Outline each blood parasite and name the species.
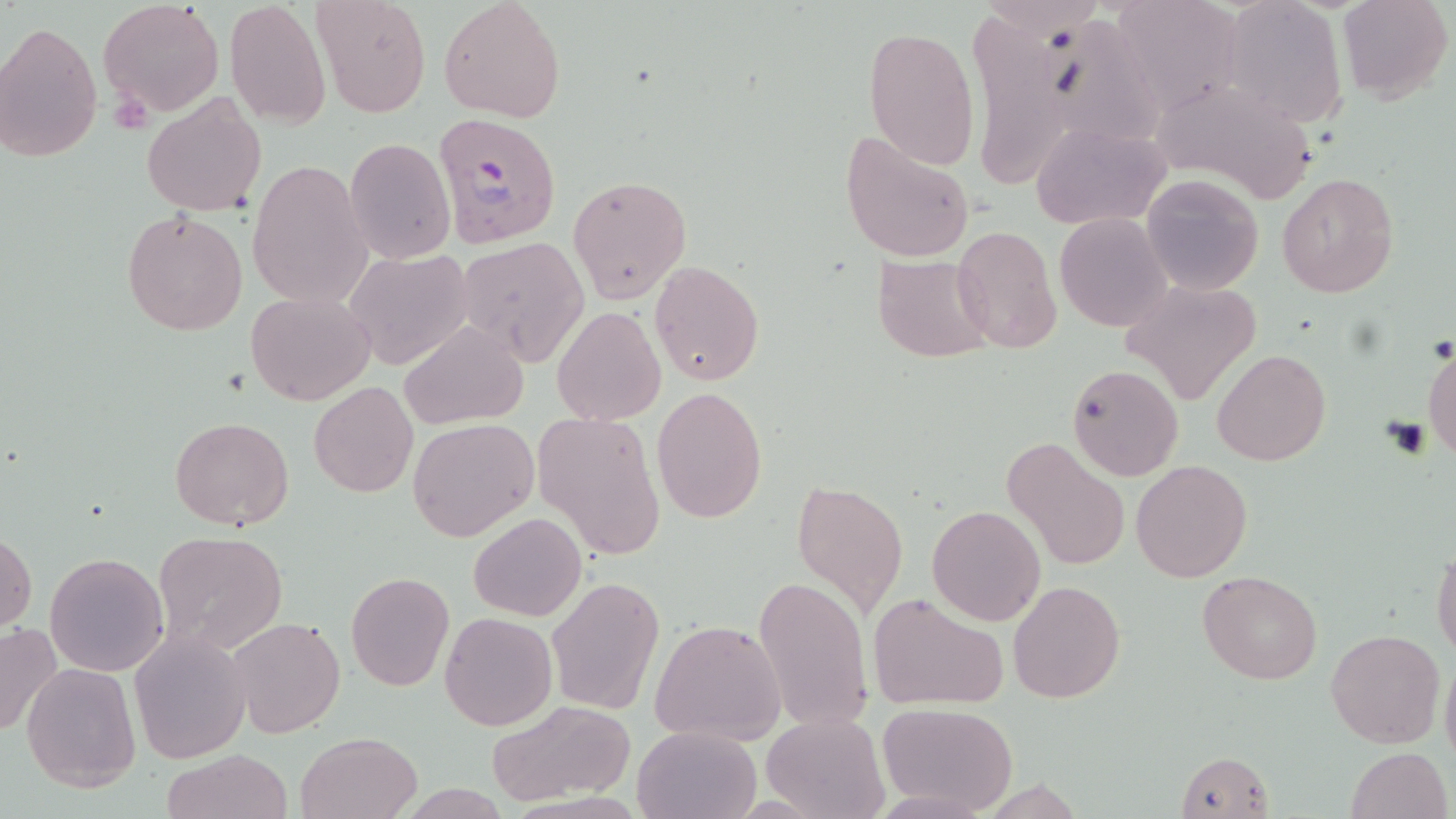
Approximate bounding boxes as (x1,y1)-(x2,y2) corner pairs in pixels.
Plasmodium falciparum-infected red blood cells: (431,110)-(561,249).
No Plasmodium ovale, Plasmodium malariae, Plasmodium vivax, Babesia divergens, or Trypanosoma brucei observed.

slide-level diagnosis = Plasmodium falciparum
preparation = thin blood film
magnification = 1000x
field of view = single
modality = light microscopy
image size = 1456×819 pixels
stain = May-Grünwald-Giemsa
platelet locations = approximate bounding boxes as (x1,y1)-(x2,y2) corner pairs in pixels: (110,88)-(157,137), (1384,416)-(1430,458)
uninfected red blood cell locations = approximate bounding boxes as (x1,y1)-(x2,y2) corner pairs in pixels: (311,0)-(430,118), (438,0)-(567,120), (1107,0)-(1241,115), (1219,0)-(1348,129), (1337,0)-(1452,105), (98,1)-(223,120), (225,1)-(331,127), (1040,12)-(1170,154), (975,20)-(1074,188), (0,21)-(103,163), (863,26)-(980,170), (142,93)-(267,217), (1160,94)-(1312,214), (1031,120)-(1171,229), (839,130)-(976,264), (344,137)-(455,264), (248,161)-(371,311), (1141,173)-(1263,295), (1276,173)-(1399,298), (567,174)-(693,303), (121,207)-(249,337), (1056,212)-(1173,331), (952,224)-(1062,353), (457,236)-(589,366), (344,250)-(472,368), (872,254)-(996,364), (648,261)-(764,386), (1121,280)-(1264,407), (247,290)-(374,405), (551,307)-(666,426), (399,320)-(530,431), (1423,343)-(1455,462), (1211,349)-(1330,466), (1067,363)-(1184,481), (309,382)-(418,498), (651,386)-(769,523), (531,410)-(665,561), (170,416)-(293,532), (406,418)-(539,542), (1003,437)-(1129,572), (1131,459)-(1253,583), (791,479)-(907,616), (927,504)-(1046,626), (468,512)-(585,622), (0,528)-(37,631), (153,530)-(289,655), (1431,546)-(1456,662), (45,552)-(167,677), (344,570)-(454,692), (1198,570)-(1322,685), (753,573)-(873,731), (546,577)-(665,715), (1008,580)-(1125,703), (868,594)-(1007,709), (440,613)-(557,730), (227,616)-(345,738), (651,619)-(786,745), (0,622)-(63,740), (1326,628)-(1445,748), (129,629)-(251,765), (1439,655)-(1456,772), (20,661)-(141,791), (483,701)-(635,805), (874,701)-(1020,816), (760,712)-(887,819), (632,724)-(763,819), (295,732)-(422,819), (1345,747)-(1452,819), (160,749)-(293,819), (1175,751)-(1274,819)